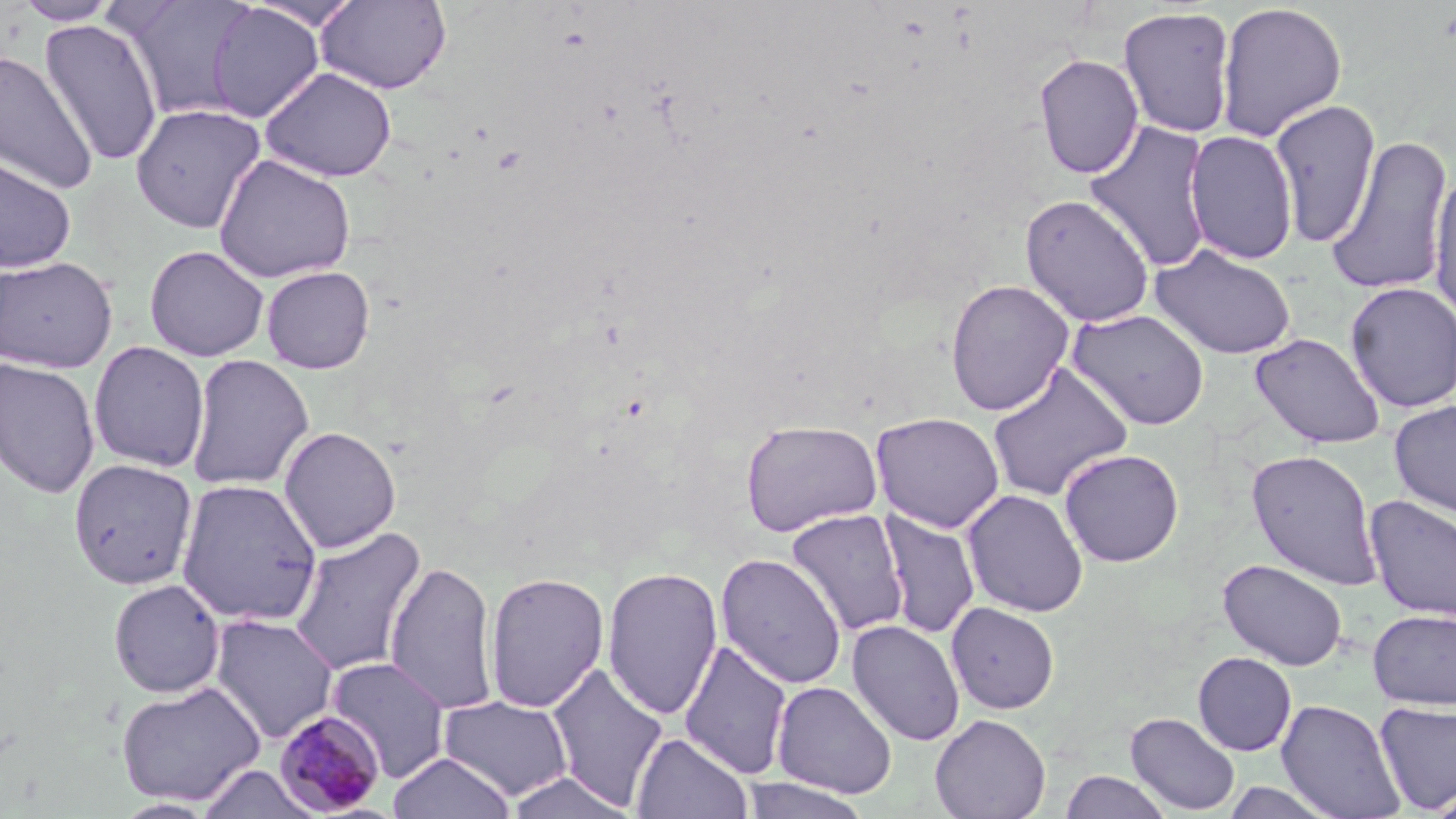

slide-level diagnosis = Plasmodium malariae
image size = 1456×819 pixels
uninfected red blood cell locations = approximate bounding boxes as [x1, y1, x2, y2] in pixels: [116, 0, 256, 121], [245, 0, 364, 31], [316, 0, 452, 94], [12, 1, 119, 26], [206, 2, 324, 123], [1215, 2, 1348, 142], [1118, 6, 1237, 138], [39, 18, 163, 167], [0, 50, 96, 194], [1033, 53, 1144, 178], [260, 67, 397, 182], [1268, 99, 1381, 249], [131, 103, 266, 234], [1083, 120, 1215, 272], [1184, 129, 1298, 265], [1326, 136, 1453, 297], [1, 153, 77, 274], [214, 153, 356, 284], [1428, 168, 1456, 324], [1019, 194, 1155, 328], [144, 244, 269, 361], [1150, 244, 1297, 360], [0, 255, 118, 373], [260, 265, 375, 374], [944, 279, 1075, 416], [1344, 281, 1456, 414], [1067, 308, 1211, 430], [1250, 332, 1385, 449], [88, 340, 210, 473], [185, 353, 314, 492], [0, 357, 101, 499], [987, 361, 1133, 503], [1389, 400, 1456, 517], [870, 411, 1005, 533], [740, 420, 883, 537], [278, 425, 402, 553], [1058, 448, 1185, 567], [1246, 449, 1383, 591], [67, 458, 198, 589], [175, 478, 323, 626], [961, 488, 1089, 618], [1363, 495, 1456, 622], [786, 508, 910, 638], [877, 508, 980, 640], [287, 525, 428, 677], [715, 552, 848, 690], [1218, 558, 1348, 671], [384, 559, 500, 715], [602, 566, 724, 720], [483, 571, 610, 713], [108, 578, 225, 698], [946, 601, 1060, 714], [1367, 609, 1456, 710], [208, 614, 339, 744], [846, 619, 965, 746], [678, 637, 793, 780], [1192, 652, 1296, 756], [325, 656, 451, 781], [545, 663, 669, 810], [115, 680, 266, 807], [771, 680, 897, 798], [438, 695, 574, 801], [1276, 698, 1406, 819], [1374, 701, 1456, 813], [1125, 711, 1240, 815], [929, 713, 1051, 819], [631, 732, 753, 819], [388, 752, 516, 819], [195, 764, 323, 819], [503, 770, 638, 818], [1060, 770, 1173, 819], [738, 776, 873, 818], [1220, 781, 1341, 819], [1425, 787, 1456, 819]
preparation = thin blood film
modality = light microscopy
field of view = single
stain = May-Grünwald-Giemsa
magnification = 1000x
Plasmodium malariae-infected red blood cell locations = approximate bounding boxes as [x1, y1, x2, y2] in pixels: [273, 709, 389, 815]